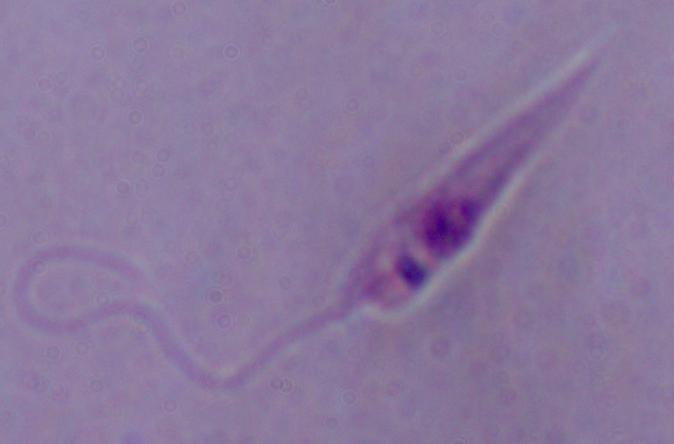
Summary:
  - Modality: photomicrograph
  - Magnification: 1000x
  - Identification: Leishmania